Report the malaria status of this cell.
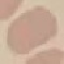

It is uninfected.

Automatically extracted cell patch, resized to 64 × 64 pixels. Acquired by smartphone through the microscope eyepiece. Giemsa stain. Thin blood smear.